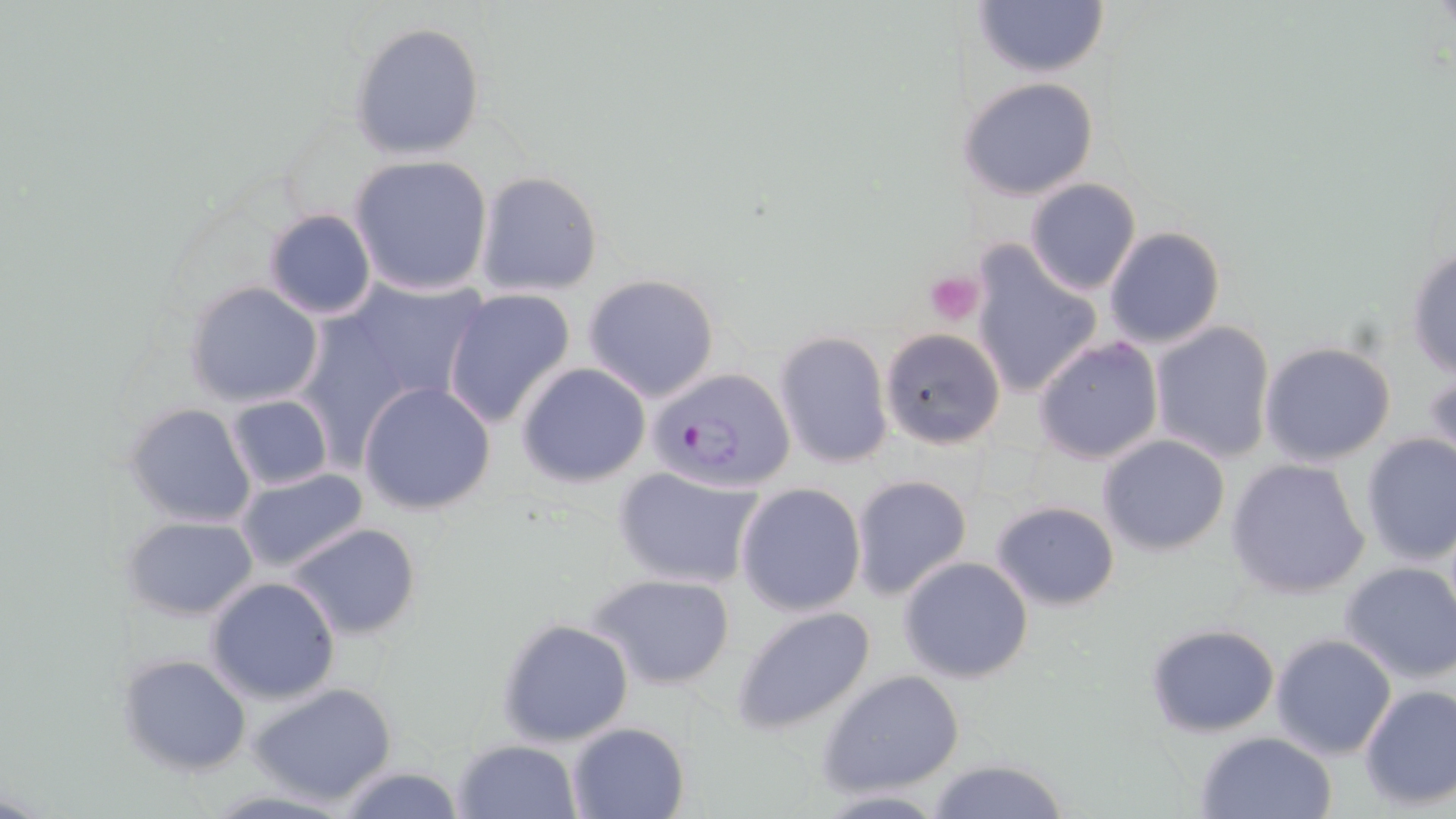 Approximate bounding boxes as (x1, y1, x2, y2) in pixels. Platelet locations: (925, 271, 985, 327). Plasmodium falciparum-infected red blood cell locations: (647, 366, 796, 494). Uninfected red blood cell locations: (969, 0, 1109, 80), (350, 21, 486, 160), (958, 77, 1100, 201), (349, 154, 494, 297), (473, 171, 603, 297), (1025, 178, 1141, 294), (264, 209, 376, 321), (1103, 225, 1226, 349), (970, 243, 1104, 400), (1405, 245, 1456, 379), (299, 272, 487, 451), (582, 273, 721, 402), (185, 280, 325, 408), (441, 288, 577, 430), (1148, 320, 1276, 462), (879, 328, 1006, 449), (773, 329, 893, 470), (1033, 336, 1164, 465), (1260, 342, 1397, 466), (515, 362, 651, 489), (1426, 366, 1456, 475), (358, 382, 497, 516), (225, 394, 331, 492), (124, 403, 257, 526), (1358, 433, 1456, 565), (1098, 435, 1230, 556), (1227, 457, 1370, 600), (613, 463, 767, 590), (234, 469, 371, 575), (850, 474, 972, 601), (735, 482, 866, 617), (989, 500, 1120, 611), (122, 515, 259, 621), (286, 522, 420, 641), (899, 555, 1036, 683), (1339, 562, 1456, 684), (590, 572, 736, 690), (207, 576, 341, 704), (731, 604, 876, 735), (498, 618, 634, 747), (1145, 623, 1282, 735), (1270, 634, 1396, 760), (129, 655, 255, 775), (818, 669, 965, 796), (249, 680, 399, 807), (1357, 683, 1455, 813), (567, 721, 691, 818), (1193, 731, 1340, 819), (453, 739, 580, 819), (924, 757, 1071, 819), (336, 765, 467, 819), (814, 790, 951, 818). Slide-level diagnosis: Plasmodium falciparum. Image is 1456×819 pixels. Optical microscopy. Thin blood film. One field of a larger specimen. Captured at 1000x magnification. May-Grünwald-Giemsa stain.